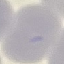
{
  "malaria_status": "uninfected",
  "stain": "Giemsa",
  "image_type": "cell patch, automatically extracted from a larger field of view and resized to 64 × 64 pixels",
  "capture": "smartphone through the microscope eyepiece",
  "preparation": "thin smear"
}